Report the malaria status of this cell.
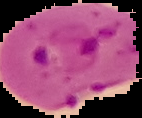

It is parasitized.

Image is 142×118 pixels. From a thin blood smear. Cell region segmented out of the field of view; the surrounding area is masked to black.